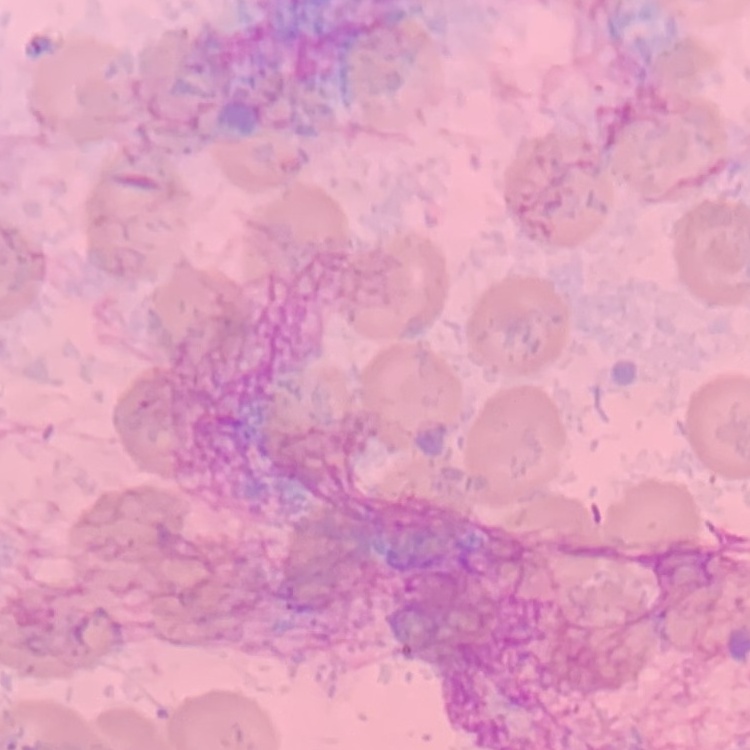

Summary:
  - Erythrocyte morphology: no rouleaux formation
  - Preparation: thin blood smear
  - Stain: Field's or Giemsa
  - Image type: square crop of a larger photomicrograph